Assess the morphology of the erythrocytes.
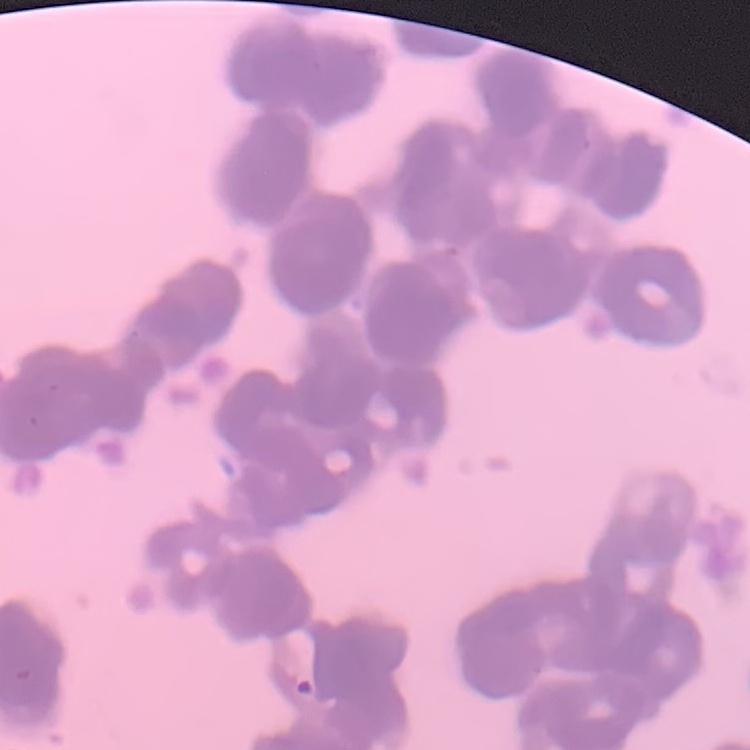

They show rouleaux formation.

Square crop of a larger photomicrograph. Thin peripheral smear. Stained with either Field's or Giemsa.